Locate every Plasmodium vivax-infected red blood cell.
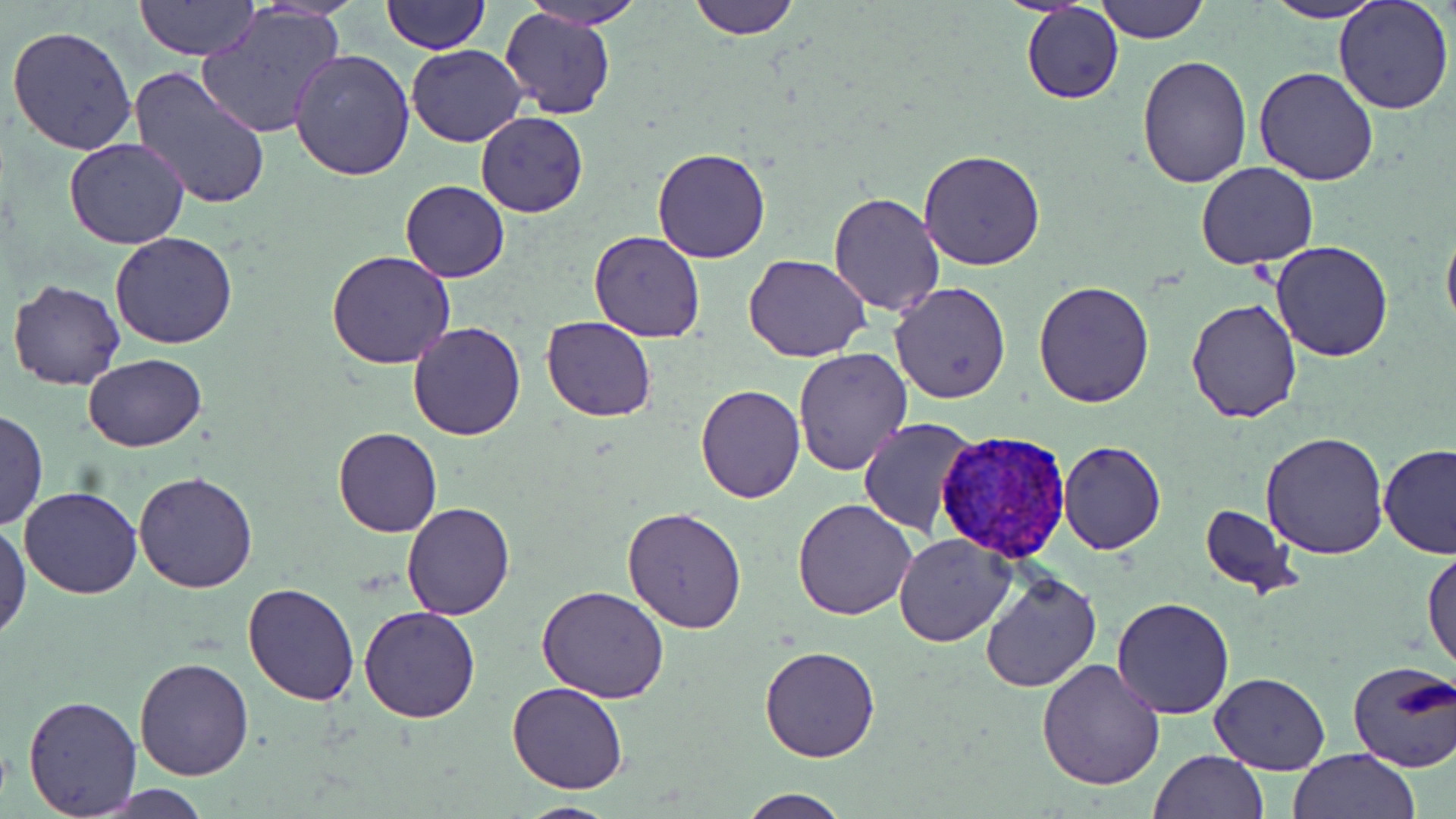

Approximate bounding boxes as (x1,y1)-(x2,y2) corner pairs in pixels.
Plasmodium vivax-infected red blood cells: (936,429)-(1072,565).

Uninfected red blood cell locations: (135,0)-(257,59), (257,0)-(363,18), (383,0)-(488,53), (522,0)-(642,29), (689,0)-(798,39), (1095,0)-(1209,44), (1333,0)-(1454,116), (1264,1)-(1387,23), (1022,2)-(1124,104), (197,3)-(348,142), (499,8)-(616,120), (6,24)-(139,156), (407,43)-(527,147), (289,49)-(415,180), (1136,57)-(1253,188), (1253,66)-(1381,185), (129,68)-(270,212), (476,112)-(588,217), (64,137)-(190,248), (652,147)-(771,263), (918,150)-(1045,270), (1196,162)-(1320,271), (400,180)-(510,282), (828,192)-(945,316), (1441,222)-(1456,337), (111,231)-(238,349), (589,231)-(705,343), (1270,241)-(1393,361), (327,249)-(458,368), (744,252)-(872,362), (7,278)-(125,390), (1033,279)-(1156,406), (889,281)-(1013,405), (1186,299)-(1302,422), (541,315)-(658,422), (408,321)-(526,440), (791,349)-(914,475), (83,354)-(206,453), (695,385)-(805,504), (1,410)-(47,532), (858,417)-(975,536), (332,427)-(442,538), (1260,431)-(1389,559), (1058,439)-(1167,556), (1378,442)-(1456,558), (134,470)-(258,593), (20,486)-(143,599), (792,498)-(919,621), (401,501)-(517,619), (622,505)-(748,632), (1198,505)-(1297,595), (0,521)-(31,641), (894,532)-(1016,647), (1422,546)-(1455,675), (979,572)-(1103,693), (243,581)-(360,704), (537,585)-(669,702), (1110,596)-(1236,720), (358,606)-(479,723), (759,645)-(883,763), (134,656)-(254,780), (1037,660)-(1165,791), (1347,660)-(1456,773), (1209,673)-(1331,775), (507,680)-(628,793), (22,694)-(141,816), (1149,749)-(1270,819), (1287,749)-(1420,819), (737,790)-(853,819), (513,800)-(623,817). Slide-level diagnosis: Plasmodium vivax. One field of a larger specimen. 1000x magnification. Light microscopy. Image is 1456×819 pixels. May-Grünwald-Giemsa-stained preparation. Thin blood film.